Assess the morphology of the erythrocytes.
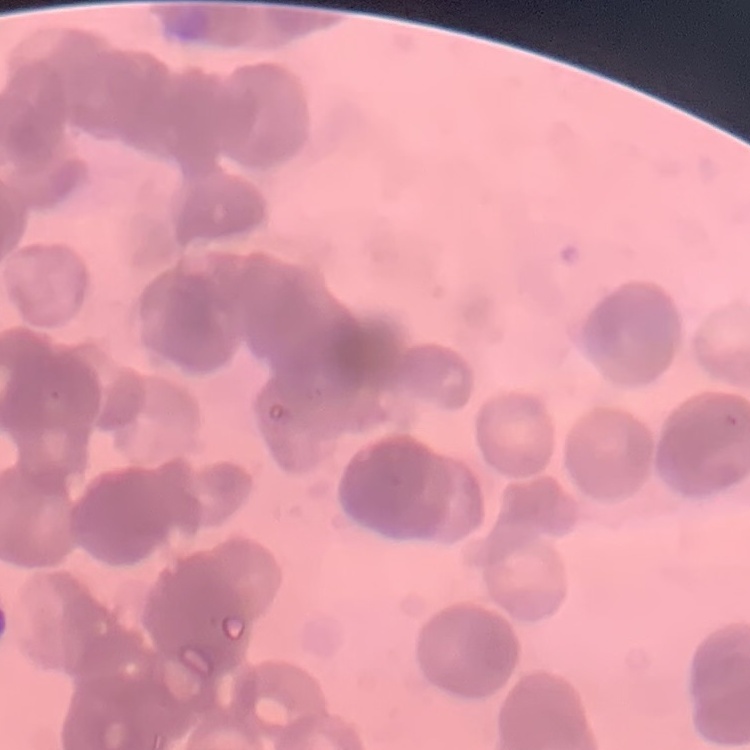

They show rouleaux formation.

Stained with either Field's or Giemsa. One tile cut from a larger photomicrograph. Thin blood smear.